Point out each leukocyte.
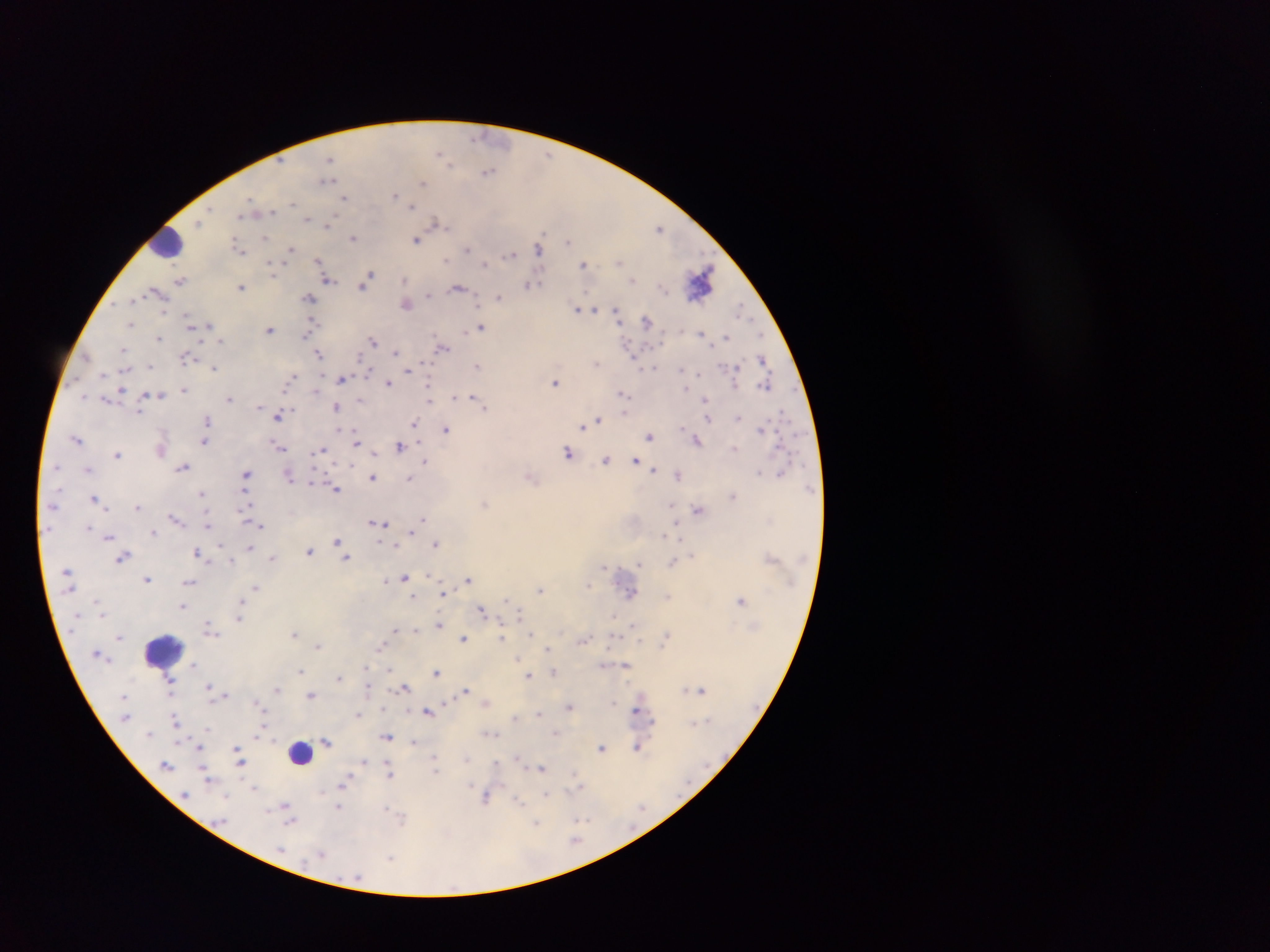

Approximate centers as {x, y} in pixels.
Leukocytes: {162, 244}, {162, 651}, {300, 754}.

Malaria parasite locations: {477, 136}, {439, 153}, {443, 154}, {549, 154}, {330, 159}, {488, 171}, {328, 180}, {423, 183}, {395, 194}, {344, 198}, {249, 201}, {292, 202}, {411, 207}, {272, 212}, {242, 219}, {307, 220}, {200, 223}, {435, 224}, {329, 225}, {442, 225}, {661, 227}, {543, 235}, {266, 239}, {353, 239}, {417, 241}, {568, 241}, {290, 248}, {468, 248}, {538, 248}, {238, 249}, {242, 250}, {511, 252}, {318, 258}, {447, 259}, {619, 262}, {487, 264}, {271, 265}, {583, 265}, {273, 270}, {370, 274}, {367, 278}, {328, 280}, {631, 280}, {405, 281}, {528, 285}, {362, 287}, {459, 287}, {241, 288}, {157, 292}, {429, 296}, {499, 296}, {310, 299}, {408, 306}, {739, 306}, {114, 307}, {576, 309}, {596, 309}, {617, 313}, {313, 321}, {647, 321}, {188, 322}, {130, 324}, {481, 326}, {210, 327}, {271, 329}, {160, 336}, {305, 337}, {726, 337}, {372, 340}, {220, 341}, {759, 341}, {200, 343}, {445, 348}, {122, 349}, {397, 351}, {320, 354}, {359, 357}, {762, 357}, {426, 361}, {597, 362}, {477, 366}, {653, 367}, {150, 368}, {214, 368}, {409, 370}, {681, 370}, {368, 372}, {698, 373}, {294, 377}, {343, 381}, {388, 383}, {764, 384}, {429, 385}, {557, 385}, {686, 385}, {121, 390}, {184, 390}, {623, 392}, {83, 395}, {453, 396}, {473, 396}, {229, 400}, {429, 400}, {486, 406}, {336, 407}, {780, 411}, {623, 412}, {277, 416}, {737, 418}, {709, 419}, {598, 420}, {415, 421}, {594, 422}, {582, 426}, {762, 428}, {415, 429}, {448, 430}, {650, 436}, {76, 439}, {697, 440}, {205, 441}, {356, 443}, {400, 447}, {321, 450}, {374, 452}, {118, 453}, {567, 453}, {606, 460}, {635, 461}, {425, 462}, {351, 465}, {182, 467}, {654, 470}, {247, 472}, {759, 472}, {780, 472}, {678, 475}, {246, 477}, {374, 478}, {409, 478}, {313, 481}, {334, 488}, {90, 493}, {203, 494}, {94, 495}, {485, 504}, {671, 504}, {138, 506}, {698, 510}, {242, 514}, {173, 517}, {424, 517}, {384, 523}, {209, 526}, {262, 526}, {678, 531}, {411, 534}, {664, 535}, {108, 536}, {337, 541}, {435, 544}, {195, 551}, {310, 553}, {121, 558}, {346, 558}, {232, 559}, {638, 563}, {606, 567}, {403, 576}, {469, 578}, {147, 579}, {385, 580}, {190, 583}, {591, 584}, {255, 588}, {542, 590}, {631, 592}, {443, 593}, {413, 597}, {506, 598}, {241, 599}, {741, 600}, {183, 607}, {481, 607}, {519, 613}, {104, 614}, {613, 614}, {239, 620}, {440, 623}, {209, 625}, {415, 630}, {393, 631}, {295, 633}, {532, 633}, {120, 637}, {464, 637}, {503, 638}, {638, 638}, {319, 646}, {381, 646}, {548, 647}, {519, 656}, {520, 661}, {193, 665}, {627, 666}, {302, 670}, {390, 671}, {436, 672}, {552, 672}, {529, 675}, {171, 678}, {339, 678}, {209, 686}, {407, 687}, {369, 688}, {277, 690}, {466, 690}, {700, 690}, {225, 694}, {310, 694}, {614, 702}, {257, 704}, {384, 707}, {569, 707}, {426, 710}, {407, 711}, {431, 711}, {358, 713}, {539, 714}, {176, 719}, {653, 720}, {207, 729}, {556, 733}, {494, 734}, {387, 737}, {327, 741}, {413, 742}, {234, 748}, {601, 748}, {639, 749}, {435, 757}, {466, 759}, {518, 759}, {365, 761}, {496, 763}, {167, 765}, {242, 766}, {542, 768}, {575, 773}, {389, 775}, {209, 782}, {343, 785}, {252, 789}, {322, 791}, {545, 793}, {226, 796}, {486, 798}, {520, 799}, {285, 806}, {339, 807}, {383, 808}, {576, 819}, {586, 819}, {292, 822}, {536, 824}, {577, 841}, {321, 854}, {391, 857}. Collected in Ghana. Single field of view. Mobile-phone photograph taken through the microscope. Thick blood film. Image is 1270×952 pixels.